Classify this cell by malaria status.
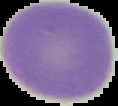
Uninfected.

From a thin blood smear. Image is 118×106 pixels. Cell region segmented out of the field of view; the surrounding area is masked to black.